Name the parasite shown.
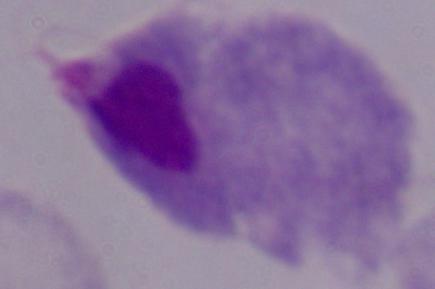
This is a trichomonad.

Summary:
  - Magnification: 1000x
  - Modality: photomicrograph